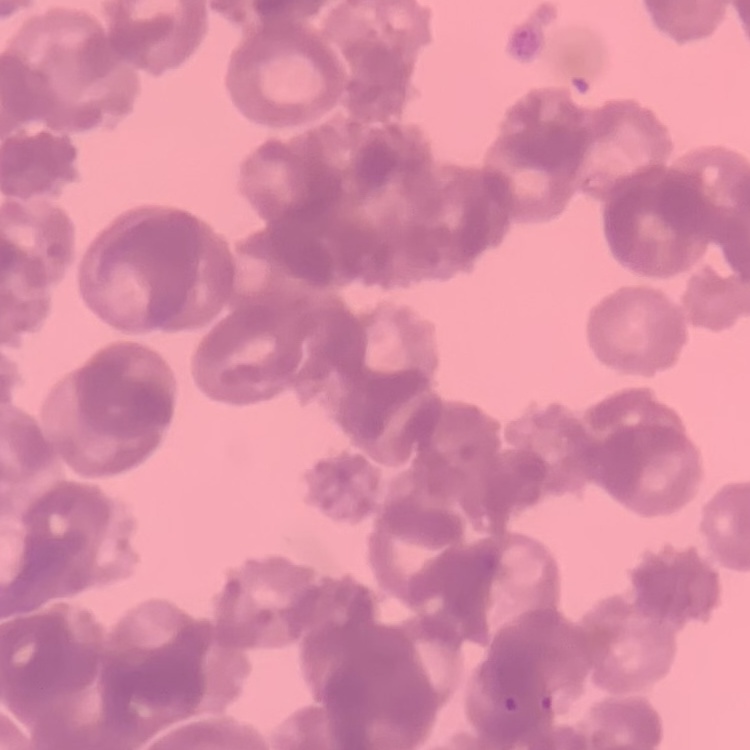
red blood cell morphology = rouleaux formation
stain = Field's or Giemsa
image type = one tile cut from a larger photomicrograph
preparation = thin peripheral smear